Assess this cell for malaria.
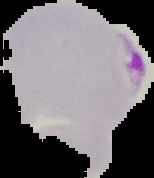

It is parasitized.

image type = segmented cell region with the area outside set to black
image size = 154×178 pixels
preparation = thin blood film